Comment on the morphology of the erythrocytes.
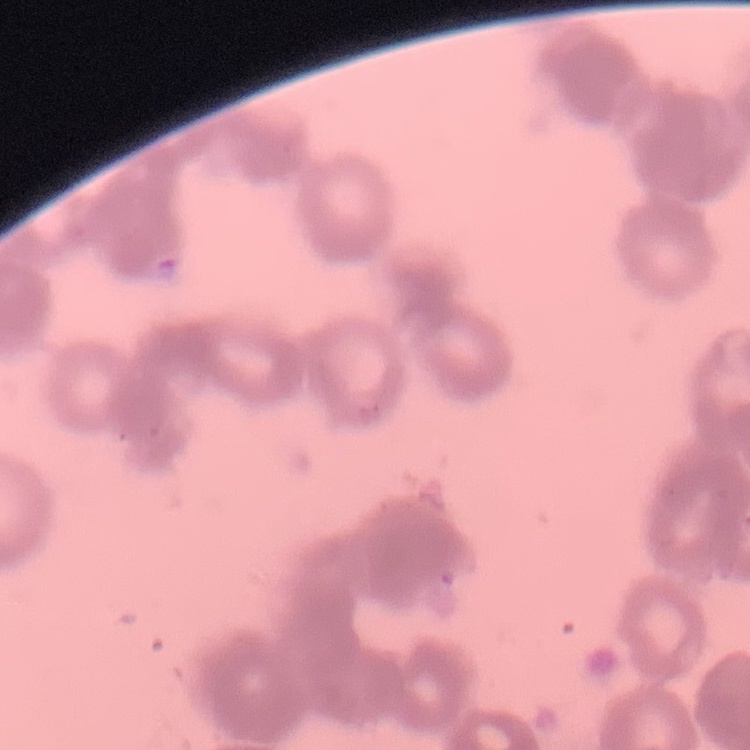

They show rouleaux formation.

Thin peripheral smear. Square crop of a larger photomicrograph. Field's or Giemsa stain.